Classify this cell by malaria status.
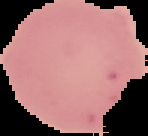

It is uninfected.

Summary:
  - Image type: segmented cell region on a black background
  - Preparation: thin blood film
  - Image size: 148×136 pixels